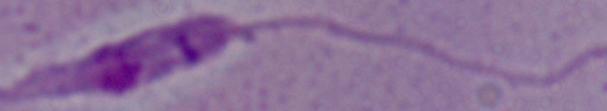
Summary:
  - Magnification: 1000x
  - Modality: micrograph
  - Identification: Leishmania